Assess this cell for malaria.
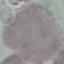

Uninfected.

Giemsa stain. Acquired by smartphone through the microscope eyepiece. Thin blood smear. Cell patch, automatically extracted from a larger field of view and resized to 64 × 64 pixels.